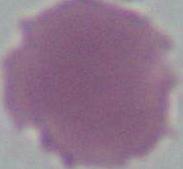
identification: erythrocyte
modality: micrograph
magnification: 1000x